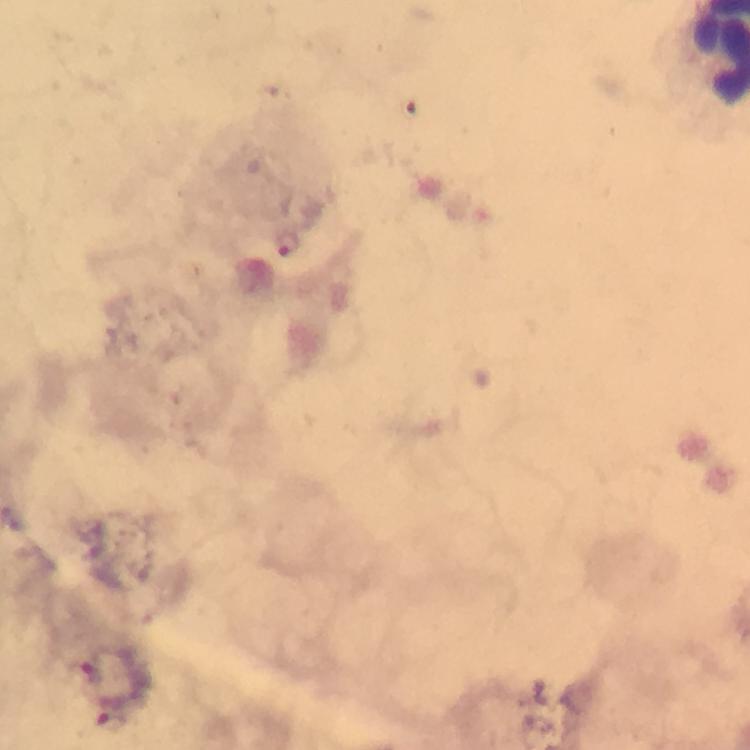
stain: Giemsa
magnification: 100x
immersion_oil: used
context: from a malaria diagnostic workup
image_size: 750×750 pixels
plasmodium_parasite_locations: 'approximate centers as {x, y} in pixels: {287, 244}, {91, 670}'
cropped_from: one field of view
preparation: thick smear
capture: smartphone camera through the microscope